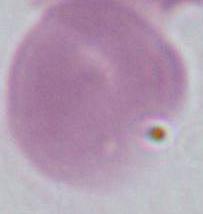
Micrograph. Captured at 1000x magnification. An erythrocyte is seen.